Locate and identify every blood parasite.
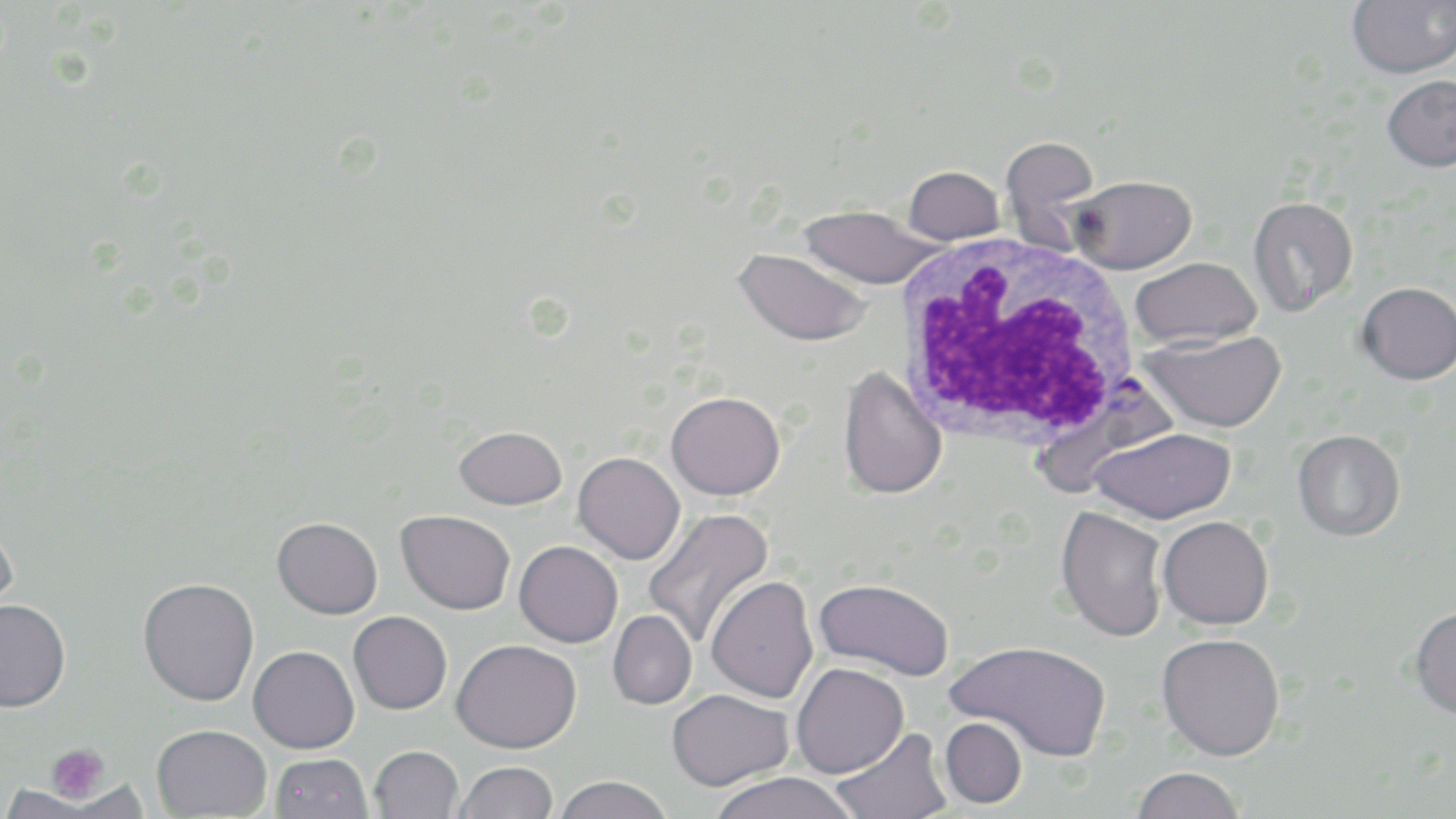
Approximate bounding boxes as [x1, y1, x2, y2] in pixels.
Plasmodium falciparum-infected red blood cells: [1034, 375, 1184, 497].
No Plasmodium ovale, Plasmodium malariae, Plasmodium vivax, Babesia divergens, or Trypanosoma brucei observed.

Summary:
  - White blood cell locations: [892, 233, 1142, 453]
  - Platelet locations: [48, 744, 110, 802]
  - Uninfected red blood cell locations: [1347, 0, 1456, 78], [1381, 75, 1456, 172], [1000, 136, 1101, 249], [903, 166, 1005, 244], [1069, 175, 1196, 274], [1248, 196, 1358, 315], [796, 205, 944, 289], [734, 248, 873, 346], [1129, 257, 1261, 348], [1356, 282, 1456, 385], [1141, 330, 1286, 432], [837, 366, 947, 500], [666, 391, 785, 500], [455, 425, 567, 509], [1091, 427, 1236, 524], [1292, 429, 1406, 541], [573, 452, 685, 564], [1055, 506, 1170, 642], [643, 508, 775, 649], [396, 509, 515, 614], [1157, 515, 1274, 629], [272, 517, 383, 619], [0, 525, 18, 625], [514, 540, 623, 647], [706, 575, 819, 703], [138, 577, 259, 705], [814, 578, 954, 680], [0, 599, 71, 712], [1409, 605, 1456, 720], [607, 610, 697, 709], [348, 611, 452, 714], [1156, 633, 1285, 760], [452, 638, 581, 753], [947, 639, 1112, 762], [248, 645, 359, 752], [791, 663, 909, 778], [666, 688, 793, 791], [940, 717, 1027, 808], [152, 723, 271, 818], [830, 727, 952, 819], [369, 745, 463, 819], [271, 753, 371, 818], [452, 761, 558, 819], [1131, 767, 1246, 819], [705, 772, 862, 819], [553, 775, 674, 819], [0, 785, 96, 819]
  - Slide-level diagnosis: Plasmodium falciparum
  - Stain: May-Grünwald-Giemsa
  - Magnification: 1000x
  - Field of view: single
  - Modality: optical microscopy
  - Preparation: thin blood smear
  - Image size: 1456×819 pixels